State which parasite is depicted.
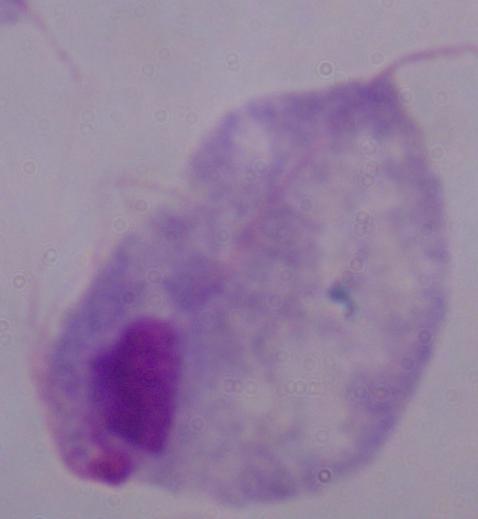
A trichomonad.

Summary:
  - Magnification: 1000x
  - Modality: micrograph